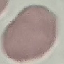

result = no malaria parasites detected
preparation = thin smear
capture = smartphone camera at the microscope eyepiece
stain = Giemsa
image type = cell patch, automatically extracted from a larger field of view and resized to 64 × 64 pixels